Assess this cell for malaria.
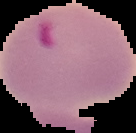
It is parasitized.

The area outside the segmented cell region is set to black. Image is 136×133 pixels. From a thin blood film.